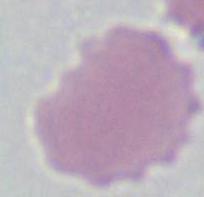
Captured at 1000x magnification. A red blood cell is seen. Micrograph.